Assess this cell for malaria.
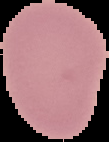
It is uninfected.

Summary:
  - Image size: 109×142 pixels
  - Preparation: thin blood film
  - Image type: cell region segmented out of the field of view; surrounding area masked to black